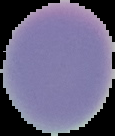
Summary:
  - Image type: segmented cell region on a black background
  - Preparation: thin blood smear
  - Image size: 115×136 pixels
  - Malaria status: uninfected